Name the cell type shown.
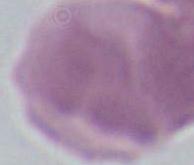
This is an erythrocyte.

modality = photomicrograph
magnification = 1000x